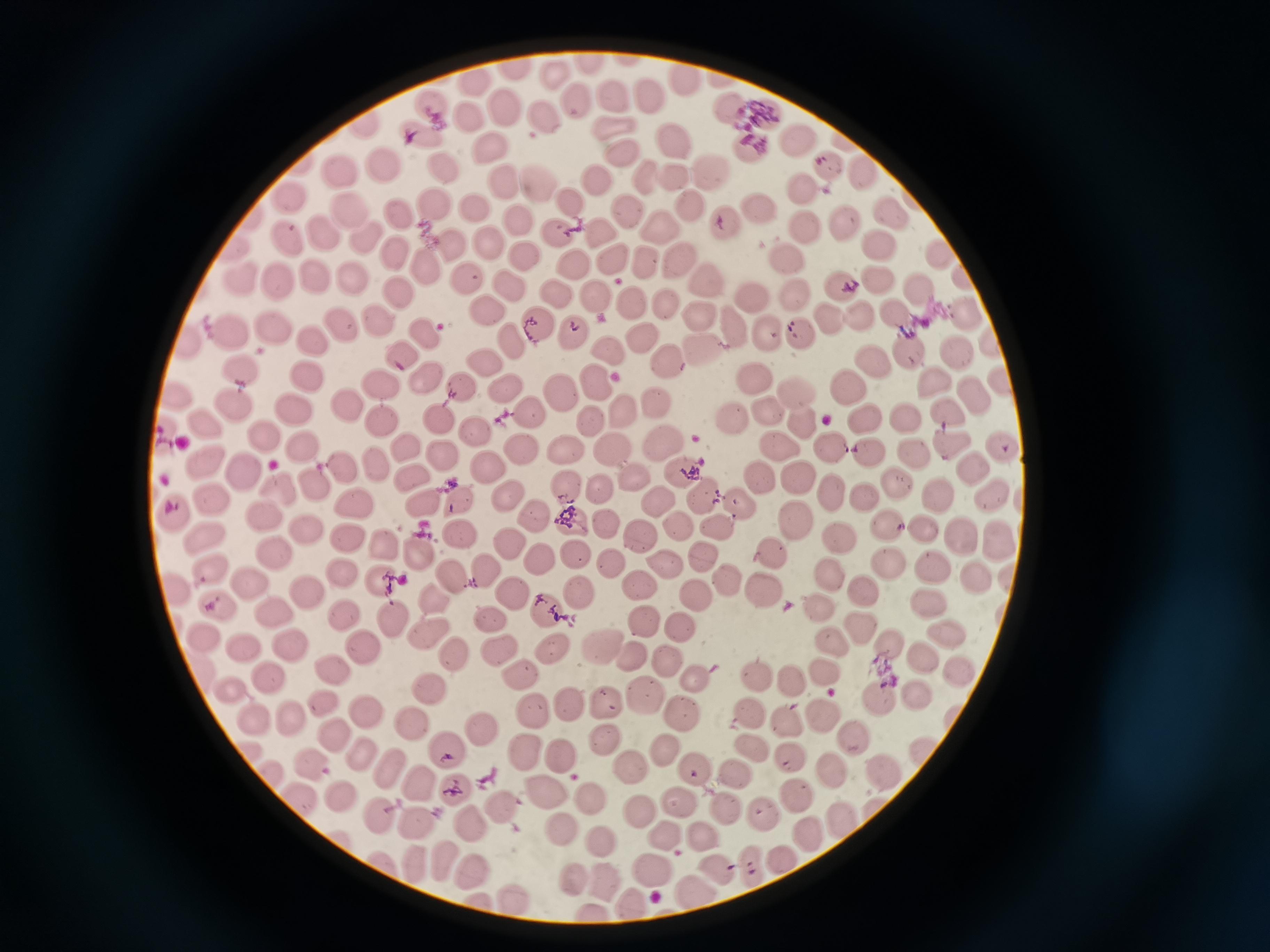
Approximate centers as {x, y} in pixels. Cell locations: {592, 66}, {516, 69}, {554, 74}, {686, 75}, {470, 81}, {646, 95}, {612, 96}, {575, 99}, {727, 103}, {431, 106}, {501, 107}, {467, 116}, {761, 116}, {540, 117}, {363, 121}, {608, 127}, {417, 132}, {798, 138}, {673, 140}, {488, 146}, {751, 149}, {619, 154}, {382, 165}, {444, 166}, {829, 168}, {710, 170}, {865, 174}, {342, 177}, {596, 177}, {677, 177}, {644, 180}, {537, 182}, {505, 183}, {288, 196}, {569, 202}, {436, 205}, {688, 206}, {760, 207}, {476, 209}, {623, 211}, {347, 212}, {398, 212}, {893, 216}, {518, 220}, {726, 223}, {846, 224}, {660, 225}, {805, 227}, {602, 229}, {557, 230}, {319, 231}, {283, 237}, {367, 237}, {488, 242}, {876, 243}, {449, 246}, {232, 249}, {397, 253}, {527, 256}, {614, 257}, {789, 258}, {944, 258}, {640, 259}, {679, 263}, {572, 266}, {423, 269}, {352, 276}, {238, 277}, {315, 278}, {465, 279}, {876, 279}, {282, 282}, {711, 282}, {839, 284}, {509, 285}, {915, 289}, {793, 290}, {554, 294}, {595, 294}, {398, 295}, {753, 297}, {631, 302}, {665, 304}, {488, 311}, {895, 311}, {967, 312}, {697, 315}, {826, 316}, {859, 316}, {378, 322}, {340, 325}, {733, 325}, {538, 327}, {272, 328}, {570, 330}, {230, 331}, {767, 331}, {800, 333}, {425, 335}, {639, 336}, {313, 338}, {186, 341}, {510, 342}, {987, 342}, {706, 348}, {908, 351}, {953, 351}, {398, 352}, {609, 352}, {668, 361}, {484, 362}, {869, 363}, {243, 368}, {309, 377}, {755, 377}, {1001, 377}, {429, 378}, {595, 381}, {379, 382}, {932, 384}, {460, 385}, {849, 385}, {505, 387}, {174, 394}, {972, 394}, {559, 395}, {794, 395}, {348, 404}, {655, 405}, {234, 407}, {294, 408}, {769, 409}, {624, 410}, {946, 412}, {528, 413}, {906, 415}, {863, 416}, {439, 419}, {730, 419}, {801, 420}, {202, 421}, {384, 421}, {588, 424}, {474, 430}, {166, 435}, {262, 435}, {660, 439}, {949, 441}, {404, 444}, {1004, 444}, {828, 446}, {303, 448}, {613, 448}, {781, 448}, {521, 450}, {568, 450}, {870, 454}, {917, 454}, {441, 457}, {200, 458}, {489, 465}, {379, 466}, {972, 466}, {343, 468}, {679, 469}, {245, 472}, {634, 474}, {760, 474}, {411, 475}, {799, 476}, {312, 483}, {899, 483}, {597, 485}, {567, 487}, {280, 490}, {830, 491}, {507, 494}, {657, 496}, {993, 496}, {702, 497}, {941, 497}, {869, 498}, {457, 499}, {212, 500}, {357, 503}, {424, 504}, {743, 504}, {173, 515}, {535, 515}, {265, 517}, {795, 519}, {574, 522}, {605, 522}, {886, 523}, {718, 525}, {678, 526}, {924, 528}, {307, 532}, {458, 532}, {959, 536}, {350, 537}, {999, 537}, {207, 538}, {642, 538}, {839, 539}, {384, 541}, {509, 542}, {774, 552}, {575, 553}, {418, 554}, {272, 556}, {703, 556}, {540, 558}, {889, 562}, {611, 563}, {661, 564}, {935, 568}, {212, 570}, {829, 570}, {486, 572}, {339, 573}, {978, 576}, {453, 577}, {380, 580}, {727, 582}, {248, 583}, {639, 587}, {174, 588}, {864, 588}, {765, 590}, {304, 591}, {579, 592}, {512, 595}, {696, 597}, {432, 600}, {929, 601}, {219, 605}, {818, 607}, {545, 609}, {276, 613}, {343, 614}, {392, 618}, {491, 620}, {641, 622}, {680, 627}, {857, 627}, {429, 632}, {201, 633}, {947, 635}, {827, 640}, {888, 640}, {294, 644}, {596, 646}, {361, 647}, {242, 648}, {497, 648}, {552, 650}, {455, 653}, {629, 657}, {925, 657}, {666, 660}, {957, 668}, {332, 670}, {825, 672}, {268, 676}, {518, 676}, {757, 676}, {696, 677}, {790, 679}, {430, 687}, {229, 690}, {644, 693}, {916, 693}, {605, 699}, {879, 699}, {570, 702}, {322, 703}, {683, 710}, {368, 712}, {533, 712}, {748, 712}, {825, 715}, {288, 717}, {406, 718}, {254, 720}, {786, 720}, {482, 726}, {332, 732}, {853, 737}, {605, 738}, {246, 745}, {753, 748}, {444, 749}, {666, 749}, {920, 752}, {526, 753}, {364, 755}, {561, 755}, {789, 758}, {312, 762}, {392, 769}, {629, 769}, {695, 770}, {830, 771}, {884, 772}, {273, 773}, {733, 774}, {420, 779}, {457, 791}, {793, 792}, {544, 794}, {342, 795}, {588, 799}, {304, 801}, {682, 805}, {724, 806}, {502, 808}, {874, 810}, {636, 812}, {381, 815}, {765, 815}, {841, 817}, {472, 820}, {415, 821}, {560, 829}, {806, 830}, {665, 837}, {703, 841}, {598, 845}, {384, 859}, {444, 860}, {781, 860}, {413, 861}, {753, 866}, {655, 867}, {473, 869}, {716, 869}, {572, 878}, {604, 883}, {695, 888}, {514, 900}, {480, 901}, {632, 904}, {597, 914}. Image is 1270×952 pixels. Photographed with a smartphone camera at the microscope eyepiece. Giemsa stain. Single field of view. Thin blood smear.